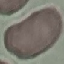
Summary:
  - Malaria status: uninfected
  - Capture: smartphone through the microscope eyepiece
  - Preparation: thin blood smear
  - Stain: Giemsa
  - Image type: automatically extracted cell patch, resized to 64 × 64 pixels